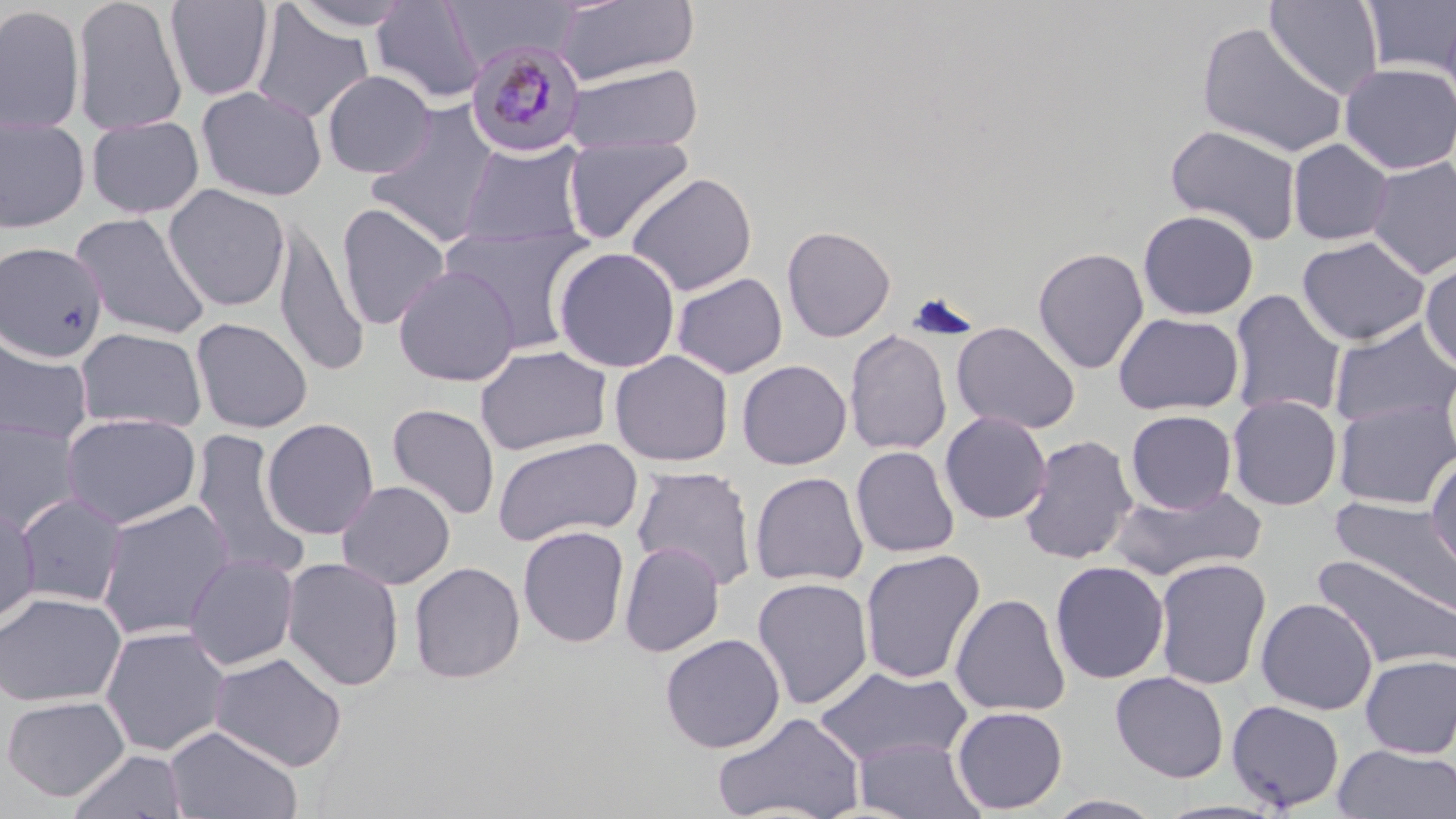
Summary:
  - Coordinate format: approximate bounding boxes as named x1/y1/x2/y2 corners in pixels
  - Plasmodium malariae-infected red blood cell locations: (x1=465, y1=38, x2=586, y2=158)
  - Uninfected red blood cell locations: (x1=72, y1=0, x2=188, y2=136), (x1=285, y1=0, x2=419, y2=31), (x1=441, y1=0, x2=576, y2=69), (x1=555, y1=0, x2=700, y2=87), (x1=1264, y1=0, x2=1384, y2=100), (x1=1361, y1=0, x2=1456, y2=78), (x1=164, y1=1, x2=275, y2=101), (x1=371, y1=1, x2=484, y2=104), (x1=250, y1=4, x2=374, y2=124), (x1=0, y1=5, x2=85, y2=134), (x1=1196, y1=21, x2=1350, y2=159), (x1=1339, y1=62, x2=1456, y2=174), (x1=565, y1=63, x2=703, y2=155), (x1=322, y1=71, x2=435, y2=178), (x1=196, y1=86, x2=327, y2=202), (x1=366, y1=101, x2=500, y2=247), (x1=0, y1=116, x2=90, y2=233), (x1=86, y1=116, x2=204, y2=219), (x1=1165, y1=124, x2=1302, y2=245), (x1=562, y1=136, x2=694, y2=246), (x1=1288, y1=138, x2=1394, y2=245), (x1=459, y1=140, x2=588, y2=249), (x1=1365, y1=157, x2=1456, y2=279), (x1=626, y1=172, x2=758, y2=296), (x1=163, y1=184, x2=290, y2=311), (x1=336, y1=203, x2=451, y2=331), (x1=1138, y1=210, x2=1259, y2=320), (x1=71, y1=212, x2=211, y2=340), (x1=273, y1=219, x2=369, y2=376), (x1=440, y1=222, x2=595, y2=354), (x1=782, y1=225, x2=896, y2=342), (x1=1297, y1=235, x2=1430, y2=346), (x1=0, y1=242, x2=108, y2=361), (x1=553, y1=246, x2=681, y2=373), (x1=1032, y1=247, x2=1149, y2=375), (x1=1421, y1=260, x2=1456, y2=373), (x1=393, y1=264, x2=521, y2=387), (x1=672, y1=272, x2=788, y2=379), (x1=1229, y1=289, x2=1346, y2=421), (x1=1113, y1=312, x2=1244, y2=416), (x1=191, y1=318, x2=312, y2=433), (x1=1329, y1=318, x2=1456, y2=431), (x1=951, y1=322, x2=1080, y2=435), (x1=74, y1=327, x2=208, y2=432), (x1=844, y1=329, x2=952, y2=456), (x1=0, y1=335, x2=93, y2=446), (x1=475, y1=345, x2=612, y2=456), (x1=610, y1=350, x2=734, y2=467), (x1=737, y1=360, x2=852, y2=470), (x1=1227, y1=394, x2=1342, y2=510), (x1=1333, y1=397, x2=1456, y2=510), (x1=387, y1=403, x2=500, y2=521), (x1=1126, y1=409, x2=1237, y2=514), (x1=939, y1=411, x2=1052, y2=524), (x1=60, y1=412, x2=202, y2=529), (x1=262, y1=417, x2=379, y2=540), (x1=0, y1=418, x2=82, y2=537), (x1=191, y1=429, x2=309, y2=580), (x1=1018, y1=435, x2=1138, y2=565), (x1=492, y1=436, x2=643, y2=546), (x1=851, y1=445, x2=960, y2=558), (x1=1425, y1=453, x2=1456, y2=577), (x1=632, y1=465, x2=758, y2=591), (x1=749, y1=471, x2=868, y2=587), (x1=336, y1=480, x2=455, y2=589), (x1=1110, y1=484, x2=1268, y2=582), (x1=15, y1=492, x2=128, y2=607), (x1=1329, y1=496, x2=1456, y2=619), (x1=95, y1=499, x2=235, y2=640), (x1=1, y1=503, x2=40, y2=629), (x1=518, y1=525, x2=630, y2=648), (x1=619, y1=541, x2=725, y2=657), (x1=859, y1=549, x2=985, y2=685), (x1=1310, y1=551, x2=1456, y2=674), (x1=184, y1=553, x2=299, y2=671), (x1=282, y1=557, x2=404, y2=691), (x1=1154, y1=557, x2=1272, y2=691), (x1=408, y1=561, x2=526, y2=683), (x1=1050, y1=561, x2=1169, y2=684), (x1=752, y1=577, x2=874, y2=709), (x1=0, y1=591, x2=126, y2=708), (x1=949, y1=593, x2=1071, y2=717), (x1=1255, y1=598, x2=1378, y2=715), (x1=99, y1=625, x2=231, y2=756), (x1=660, y1=633, x2=785, y2=753), (x1=209, y1=652, x2=348, y2=772), (x1=1359, y1=654, x2=1456, y2=759), (x1=814, y1=665, x2=973, y2=768), (x1=1110, y1=671, x2=1229, y2=783), (x1=1, y1=694, x2=130, y2=802), (x1=1226, y1=700, x2=1345, y2=812), (x1=952, y1=706, x2=1067, y2=814), (x1=713, y1=711, x2=866, y2=819), (x1=164, y1=725, x2=303, y2=819), (x1=852, y1=736, x2=984, y2=818), (x1=1332, y1=744, x2=1456, y2=819), (x1=66, y1=749, x2=188, y2=819), (x1=1045, y1=794, x2=1166, y2=818), (x1=1152, y1=799, x2=1289, y2=819)
  - Slide-level diagnosis: Plasmodium malariae
  - Image size: 1456×819 pixels
  - Preparation: thin blood film
  - Magnification: 1000x
  - Field of view: one of a larger specimen
  - Stain: May-Grünwald-Giemsa
  - Modality: optical microscopy